Comment on the morphology of the erythrocytes.
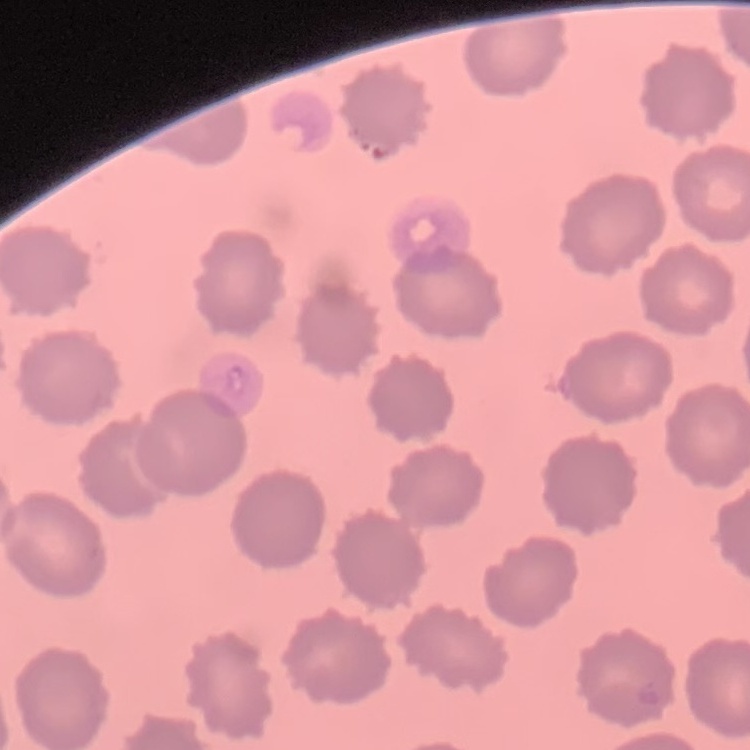
No rouleaux formation.

Thin peripheral smear. Field's or Giemsa stain. One tile cut from a larger photomicrograph.